Outline each blood parasite and name the species.
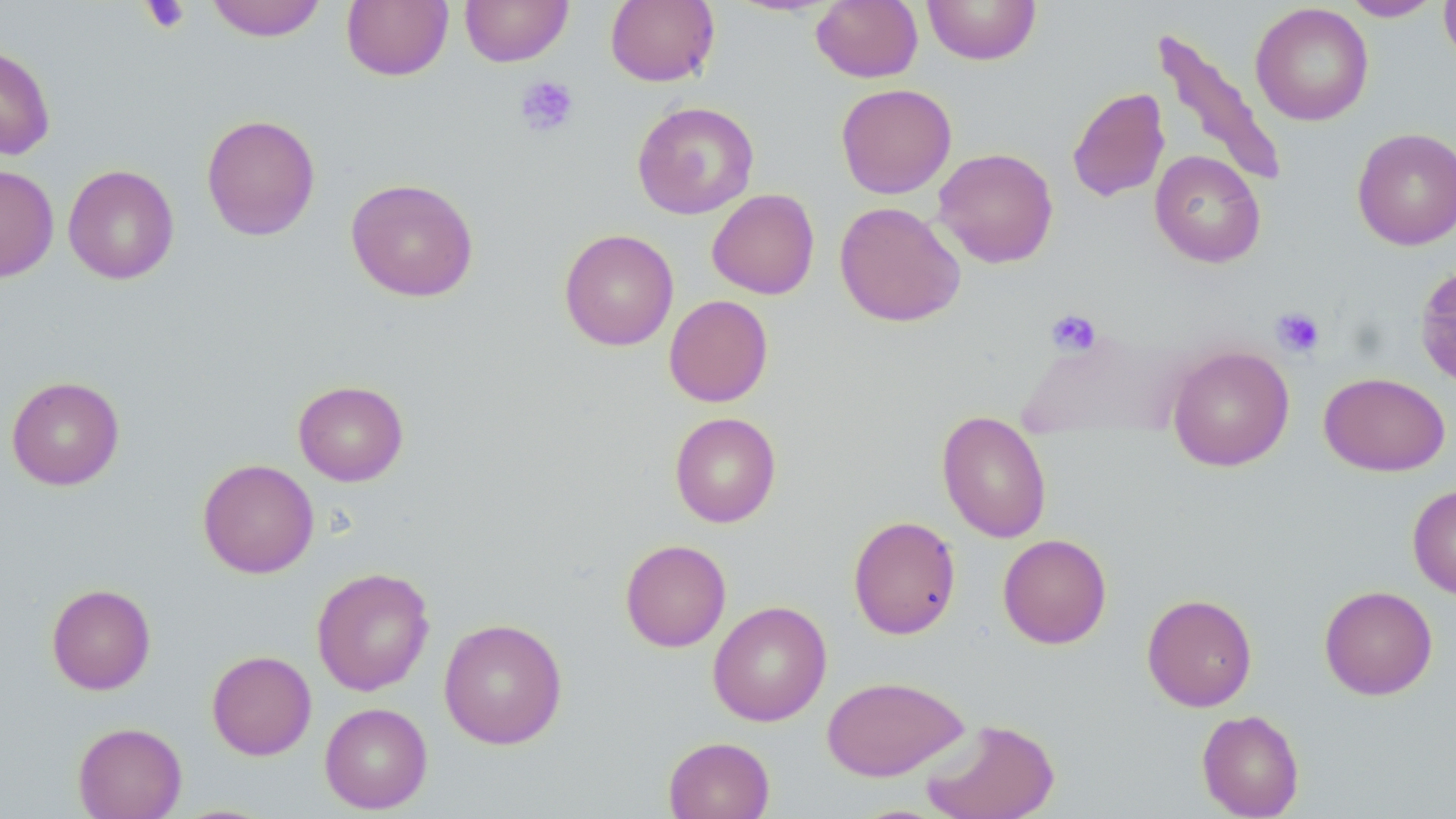
No blood parasites observed.

Summary:
  - Coordinate format: approximate bounding boxes as (x1, y1, x2, y2) in pixels
  - Platelet locations: (140, 0, 190, 34), (514, 75, 579, 138), (1271, 306, 1325, 359), (1045, 308, 1102, 357)
  - Uninfected red blood cell locations: (206, 0, 327, 41), (341, 0, 453, 81), (459, 0, 573, 66), (605, 0, 720, 87), (811, 0, 922, 83), (922, 0, 1041, 65), (1340, 0, 1443, 22), (1439, 0, 1456, 67), (1250, 3, 1373, 126), (1151, 27, 1287, 190), (0, 44, 56, 161), (835, 83, 957, 198), (1067, 87, 1170, 203), (632, 101, 759, 219), (201, 113, 321, 241), (1352, 127, 1456, 250), (933, 147, 1059, 268), (1149, 150, 1266, 268), (0, 165, 59, 282), (63, 165, 179, 284), (345, 177, 479, 302), (706, 189, 820, 299), (834, 201, 965, 327), (558, 228, 679, 351), (1414, 262, 1456, 391), (663, 294, 774, 407), (1167, 345, 1294, 472), (1319, 372, 1450, 476), (6, 376, 125, 490), (293, 380, 409, 486), (937, 410, 1052, 543), (669, 412, 781, 527), (198, 459, 319, 578), (1407, 483, 1456, 600), (847, 515, 961, 640), (998, 533, 1112, 649), (620, 539, 731, 652), (311, 567, 435, 696), (46, 583, 156, 694), (1319, 585, 1438, 700), (1142, 593, 1257, 712), (708, 600, 832, 726), (439, 618, 567, 750), (206, 650, 317, 760), (822, 675, 970, 781), (319, 702, 433, 814), (1196, 709, 1305, 819), (921, 717, 1060, 819), (73, 722, 187, 819), (663, 736, 775, 819)
  - Slide-level diagnosis: negative for blood parasites
  - Magnification: 1000x
  - Field of view: single
  - Modality: optical microscopy
  - Stain: May-Grünwald-Giemsa
  - Preparation: thin blood film
  - Image size: 1456×819 pixels